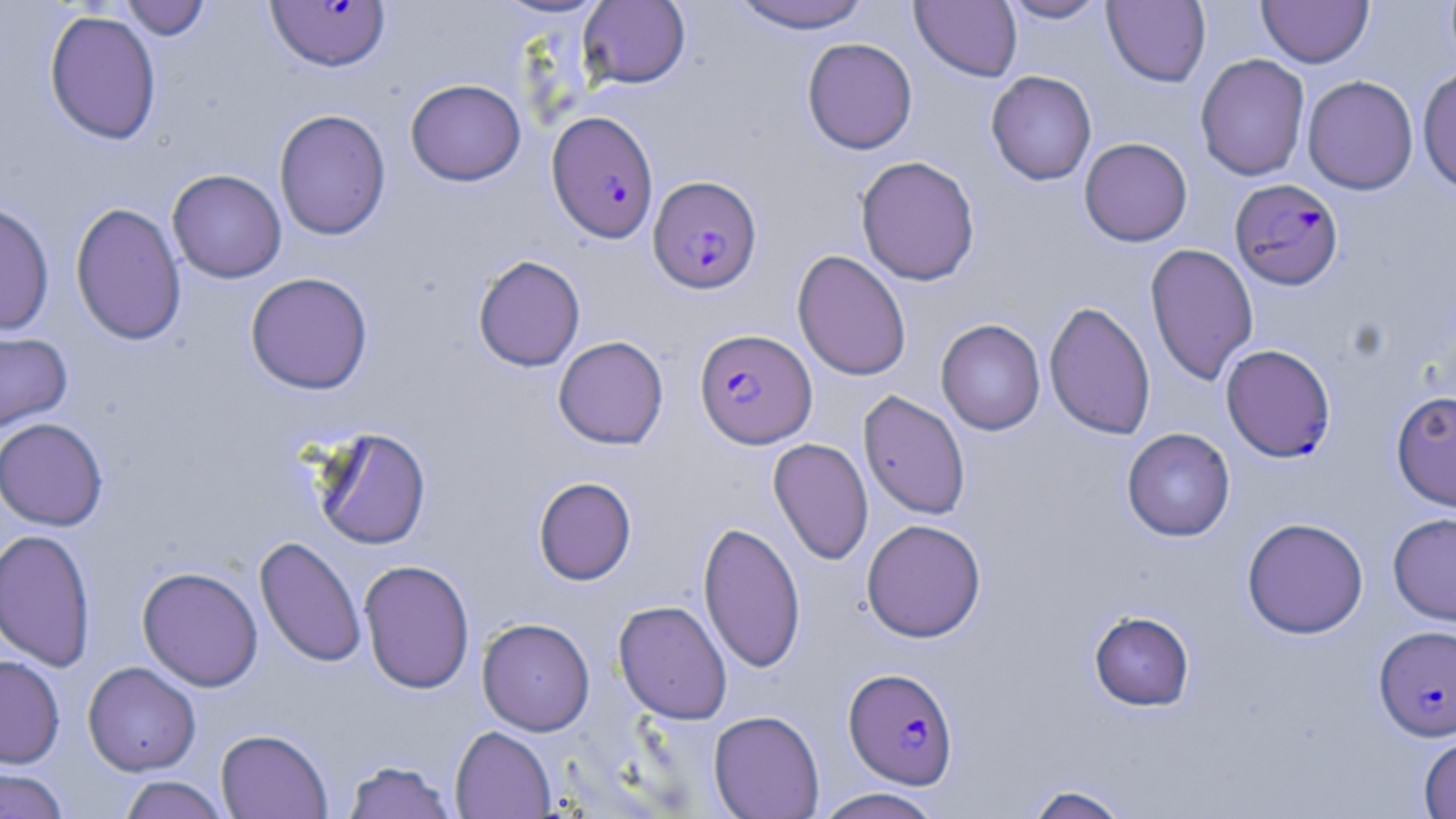

{
  "slide_level_diagnosis": "Plasmodium falciparum",
  "magnification": "1000x",
  "plasmodium_falciparum_infected_red_blood_cell_locations_subset": "approximate bounding boxes as named x1/y1/x2/y2 corners in pixels: (x1=265, y1=0, x2=391, y2=73), (x1=546, y1=111, x2=659, y2=242), (x1=648, y1=175, x2=762, y2=295), (x1=1230, y1=178, x2=1344, y2=290), (x1=694, y1=328, x2=817, y2=448), (x1=1374, y1=625, x2=1456, y2=741), (x1=843, y1=667, x2=958, y2=789)",
  "uninfected_red_blood_cell_locations_subset": "approximate bounding boxes as named x1/y1/x2/y2 corners in pixels: (x1=120, y1=0, x2=212, y2=40), (x1=492, y1=0, x2=612, y2=19), (x1=726, y1=0, x2=874, y2=33), (x1=910, y1=0, x2=1022, y2=82), (x1=999, y1=0, x2=1111, y2=23), (x1=1102, y1=0, x2=1211, y2=88), (x1=1257, y1=0, x2=1374, y2=67), (x1=579, y1=1, x2=691, y2=89), (x1=44, y1=10, x2=162, y2=145), (x1=802, y1=37, x2=918, y2=155), (x1=1195, y1=54, x2=1310, y2=181), (x1=1417, y1=66, x2=1456, y2=195), (x1=986, y1=70, x2=1097, y2=186), (x1=1302, y1=76, x2=1418, y2=195), (x1=405, y1=78, x2=526, y2=186), (x1=274, y1=109, x2=391, y2=241), (x1=1079, y1=137, x2=1192, y2=246), (x1=856, y1=155, x2=980, y2=285), (x1=167, y1=169, x2=286, y2=283), (x1=0, y1=200, x2=55, y2=336), (x1=70, y1=201, x2=186, y2=346), (x1=1145, y1=243, x2=1259, y2=386), (x1=792, y1=250, x2=911, y2=381), (x1=473, y1=255, x2=585, y2=372), (x1=245, y1=272, x2=373, y2=395), (x1=1044, y1=300, x2=1156, y2=440), (x1=935, y1=319, x2=1046, y2=435), (x1=0, y1=328, x2=73, y2=434), (x1=553, y1=336, x2=669, y2=449), (x1=1391, y1=389, x2=1456, y2=512), (x1=859, y1=390, x2=971, y2=520), (x1=0, y1=417, x2=108, y2=531), (x1=311, y1=426, x2=432, y2=549), (x1=1121, y1=428, x2=1236, y2=541), (x1=769, y1=438, x2=873, y2=565), (x1=533, y1=477, x2=637, y2=585), (x1=1388, y1=512, x2=1456, y2=627), (x1=1242, y1=517, x2=1368, y2=639), (x1=861, y1=518, x2=986, y2=643), (x1=698, y1=520, x2=806, y2=673), (x1=0, y1=528, x2=96, y2=672), (x1=255, y1=536, x2=366, y2=668), (x1=358, y1=559, x2=475, y2=694), (x1=137, y1=566, x2=264, y2=691), (x1=613, y1=600, x2=732, y2=723), (x1=1089, y1=610, x2=1195, y2=711), (x1=477, y1=617, x2=595, y2=735), (x1=0, y1=655, x2=65, y2=768), (x1=83, y1=661, x2=201, y2=776), (x1=708, y1=710, x2=825, y2=819), (x1=450, y1=726, x2=556, y2=818), (x1=216, y1=729, x2=333, y2=818), (x1=1418, y1=733, x2=1456, y2=819), (x1=341, y1=759, x2=457, y2=819), (x1=0, y1=768, x2=70, y2=818), (x1=117, y1=775, x2=231, y2=818), (x1=1021, y1=783, x2=1134, y2=819), (x1=814, y1=787, x2=944, y2=819)",
  "field_of_view": "one of a larger specimen",
  "preparation": "thin blood smear",
  "image_size": "1456×819 pixels",
  "stain": "May-Grünwald-Giemsa",
  "modality": "optical microscopy"
}